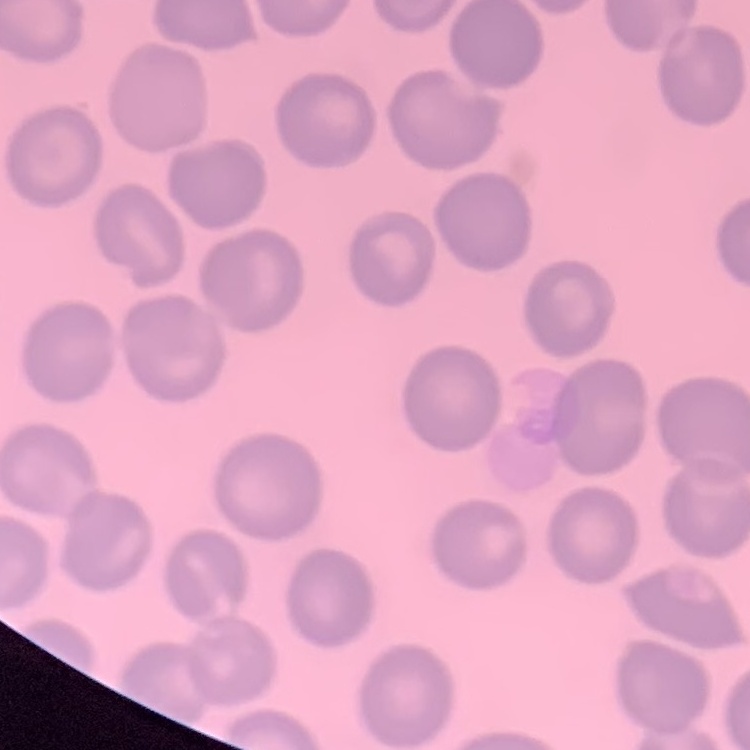

erythrocyte morphology = no rouleaux formation
preparation = thin blood smear
image type = square crop of a larger photomicrograph
stain = Field's or Giemsa